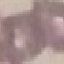

Summary:
  - Result: negative for malaria parasites
  - Preparation: thin blood smear
  - Capture: smartphone camera at the microscope eyepiece
  - Image type: cell patch, automatically extracted from a larger field of view and resized to 64 × 64 pixels
  - Stain: Giemsa